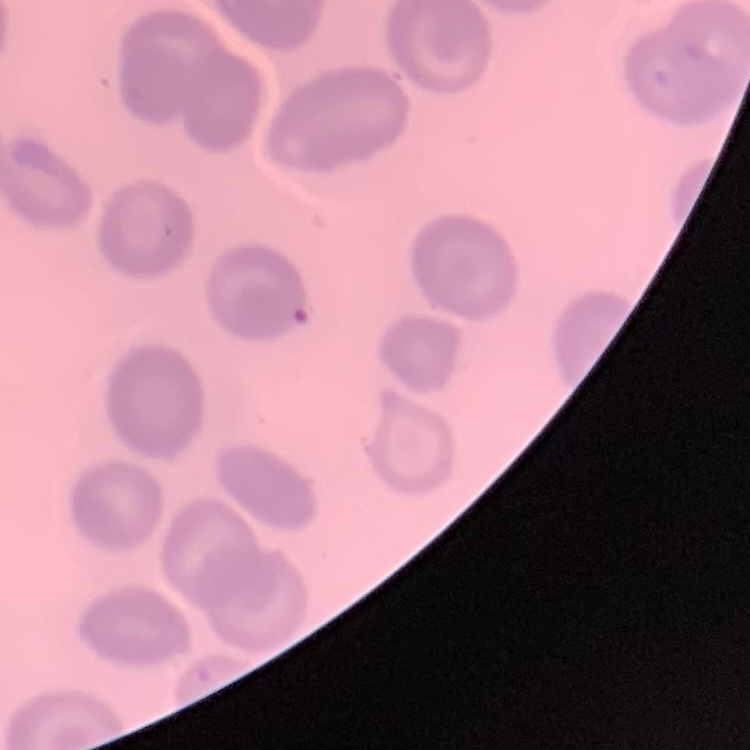

Summary:
  - Erythrocyte morphology: no rouleaux formation
  - Image type: square crop of a larger photomicrograph
  - Stain: Field's or Giemsa
  - Preparation: thin peripheral smear